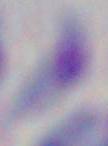
Captured at 1000x magnification. Photomicrograph. Toxoplasma gondii is shown.